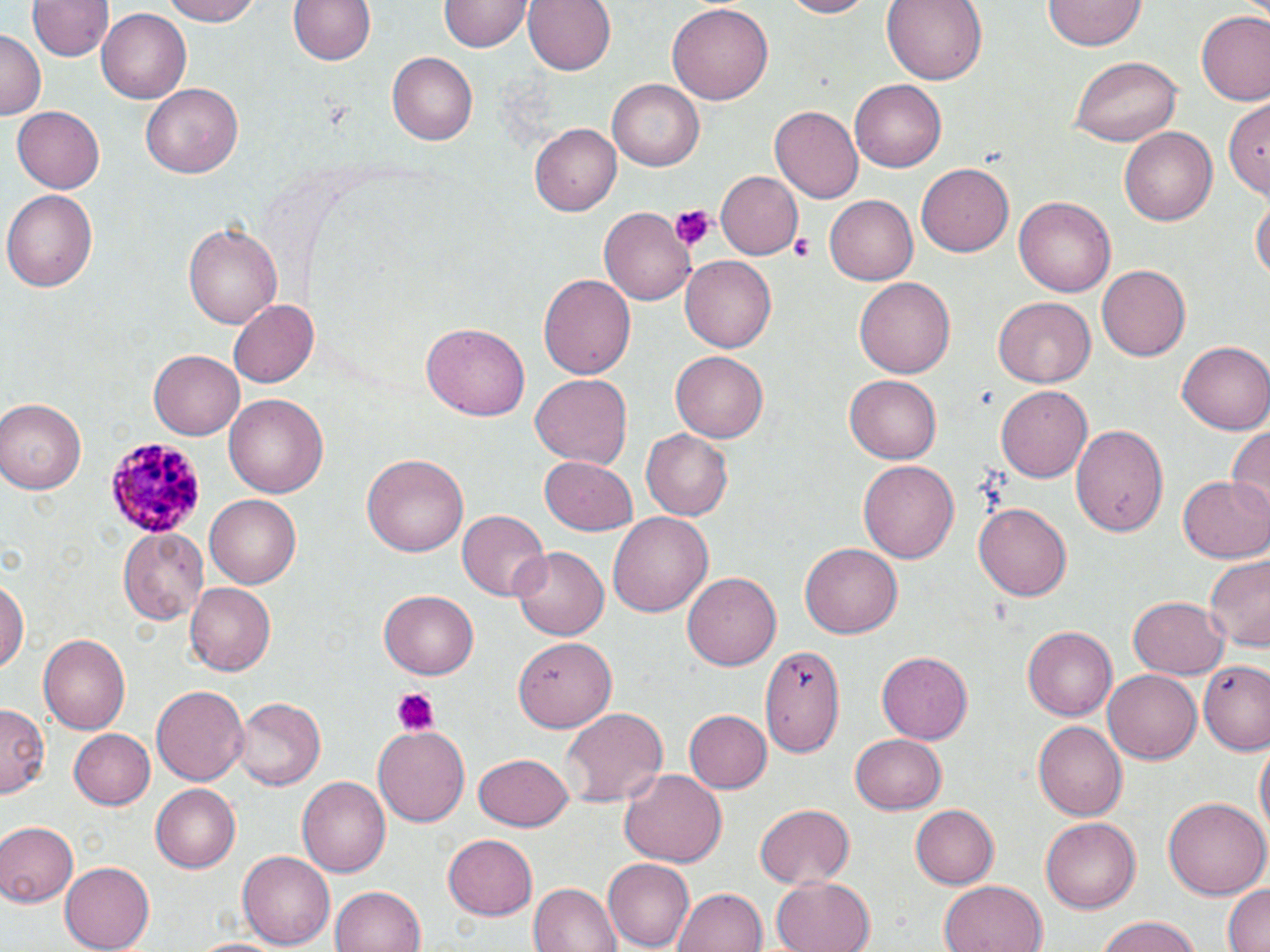

Summary:
  - Coordinate format: approximate bounding boxes as (x1,y1)-(x2,y2) corner pairs in pixels
  - Uninfected red blood cell locations: (161,0)-(268,26), (286,0)-(379,69), (522,0)-(616,76), (779,0)-(879,19), (883,0)-(987,85), (1045,0)-(1143,52), (29,1)-(113,64), (440,1)-(530,53), (670,3)-(773,105), (100,7)-(192,103), (1197,13)-(1270,108), (1,30)-(42,119), (388,53)-(478,145), (1070,55)-(1182,146), (849,77)-(946,169), (610,79)-(704,170), (140,83)-(244,180), (1224,92)-(1270,201), (10,107)-(105,193), (771,107)-(861,204), (530,122)-(622,215), (1120,124)-(1216,224), (916,162)-(1014,258), (715,170)-(802,260), (3,188)-(100,292), (1252,194)-(1269,283), (1015,195)-(1117,299), (823,196)-(918,285), (600,209)-(696,304), (182,219)-(282,332), (680,256)-(777,353), (1097,265)-(1189,361), (540,271)-(637,380), (854,277)-(957,379), (992,296)-(1095,388), (229,298)-(318,389), (420,323)-(530,422), (1178,339)-(1270,434), (671,349)-(768,441), (148,350)-(244,439), (845,374)-(942,465), (529,375)-(632,469), (995,385)-(1093,483), (224,392)-(330,497), (1,398)-(87,493), (1226,421)-(1269,522), (1071,424)-(1169,537), (639,430)-(732,520), (363,454)-(468,557), (540,455)-(638,535), (858,460)-(959,564), (1181,475)-(1270,562), (204,493)-(304,589), (975,502)-(1071,602), (457,510)-(548,600), (608,513)-(712,620), (118,525)-(210,622), (800,544)-(902,640), (511,547)-(609,640), (1205,552)-(1270,653), (1,572)-(28,682), (682,572)-(781,672), (184,583)-(274,676), (379,589)-(480,680), (1128,595)-(1228,679), (1023,626)-(1116,720), (39,632)-(131,735), (516,637)-(616,734), (757,642)-(847,758), (878,651)-(972,744), (1198,663)-(1270,754), (1103,668)-(1201,762), (151,684)-(249,784), (231,697)-(326,790), (0,707)-(49,797), (561,707)-(666,810), (684,709)-(771,793), (1034,719)-(1130,820), (372,722)-(469,824), (70,728)-(156,809), (849,733)-(945,814), (1254,737)-(1268,847), (473,753)-(575,832), (618,770)-(726,868), (295,774)-(390,876), (151,785)-(241,873), (1162,797)-(1268,902), (754,802)-(854,888), (912,802)-(1001,889), (1040,817)-(1138,913), (0,820)-(79,906), (443,831)-(538,920), (238,849)-(338,949), (600,859)-(695,950), (59,862)-(154,952), (772,877)-(876,952), (942,878)-(1047,952), (529,880)-(623,952), (1220,882)-(1270,952), (329,885)-(428,952), (673,887)-(767,952), (1092,917)-(1208,952), (184,937)-(288,952)
  - Platelet locations: (669,206)-(714,250), (789,231)-(816,261), (392,688)-(439,735)
  - Plasmodium malariae-infected red blood cell locations: (107,436)-(204,540)
  - Slide-level diagnosis: Plasmodium malariae
  - Image size: 1270×952 pixels
  - Modality: optical microscopy
  - Stain: May-Grünwald-Giemsa
  - Preparation: thin blood smear
  - Magnification: 1000x
  - Field of view: one of a larger specimen